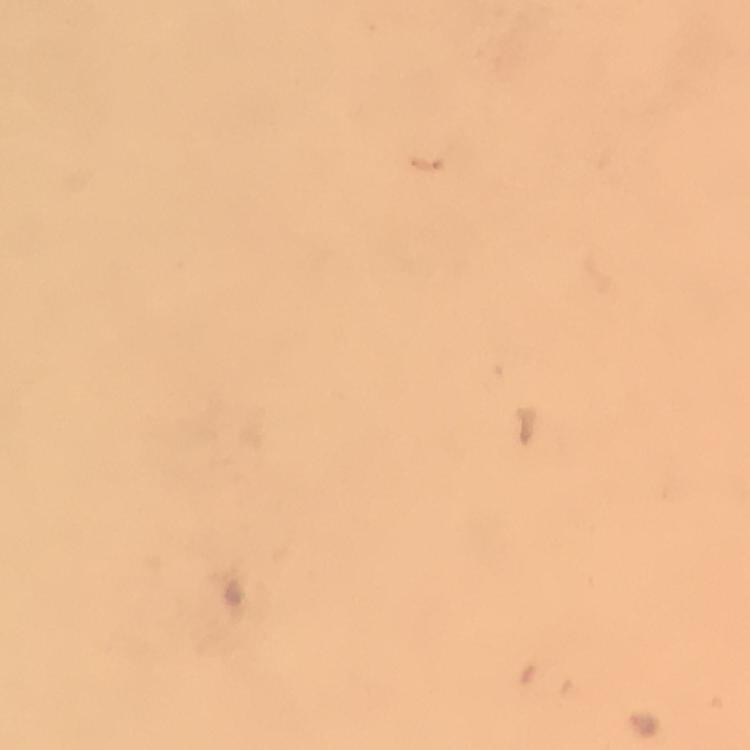 Approximate centers as [x, y] in pixels. Malaria parasite locations: [646, 724]. Smartphone photograph taken through a microscope. At 100x magnification. A crop from one field of view. Thick smear. Immersion oil was used. From a malaria diagnostic workup. Image is 750×750 pixels. Giemsa-stained preparation.